State which parasite is depicted.
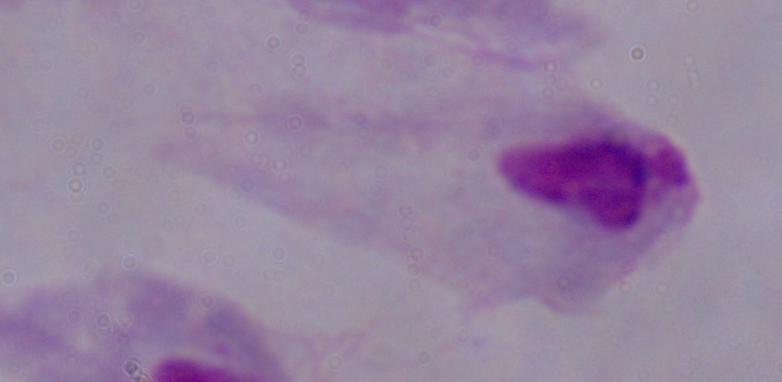

This is a trichomonad.

1000x magnification. Micrograph.